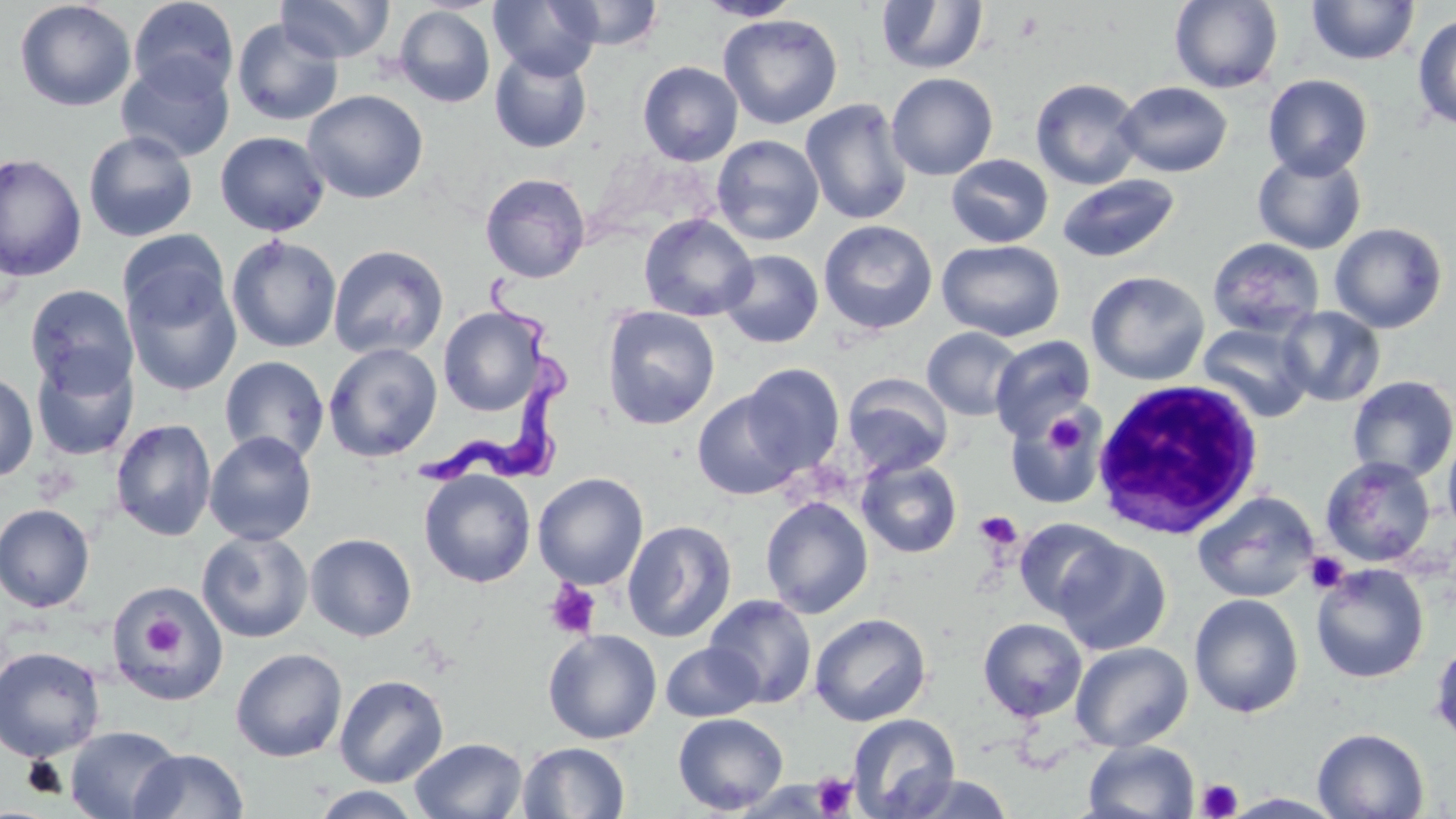
slide_level_diagnosis: Trypanosoma brucei
uninfected_red_blood_cell_locations: 'approximate bounding boxes as (x1, y1, x2, y2) in pixels: (127, 0, 240, 100), (276, 0, 393, 62), (489, 0, 602, 81), (553, 0, 665, 50), (696, 0, 804, 21), (15, 1, 136, 112), (876, 1, 989, 75), (1168, 1, 1284, 93), (1306, 1, 1420, 65), (393, 5, 495, 108), (1412, 12, 1456, 131), (718, 13, 843, 129), (232, 18, 344, 127), (489, 50, 593, 153), (116, 55, 235, 163), (637, 61, 743, 166), (886, 72, 998, 180), (1263, 74, 1373, 179), (1030, 77, 1145, 190), (1115, 81, 1233, 177), (302, 90, 428, 204), (800, 99, 913, 226), (83, 130, 198, 242), (215, 131, 330, 237), (712, 135, 824, 246), (0, 152, 87, 282), (1252, 152, 1367, 254), (945, 154, 1054, 248), (480, 172, 590, 283), (1057, 174, 1180, 264), (639, 213, 758, 322), (819, 220, 938, 335), (1329, 222, 1448, 333), (118, 230, 231, 331), (226, 235, 342, 352), (1207, 237, 1325, 339), (936, 239, 1064, 342), (328, 244, 448, 360), (719, 250, 824, 349), (124, 269, 242, 396), (1086, 270, 1210, 386), (25, 285, 138, 394), (602, 305, 720, 430), (1277, 305, 1387, 407), (438, 306, 548, 416), (1198, 323, 1314, 422), (922, 327, 1023, 420), (989, 335, 1096, 440), (323, 342, 442, 462), (31, 351, 139, 462), (218, 356, 330, 463), (740, 363, 845, 475), (0, 371, 38, 483), (841, 373, 953, 478), (1347, 375, 1456, 482), (692, 390, 804, 501), (1005, 411, 1105, 510), (110, 419, 217, 541), (204, 430, 317, 546), (1442, 432, 1456, 536), (1320, 456, 1436, 567), (856, 458, 963, 558), (419, 469, 536, 588), (532, 473, 649, 590), (1192, 491, 1319, 603), (760, 496, 874, 618), (0, 503, 95, 612), (1013, 517, 1124, 621), (622, 519, 737, 643), (197, 529, 313, 643), (305, 533, 417, 641), (1054, 538, 1171, 656), (1311, 562, 1429, 684), (106, 577, 232, 705), (1189, 593, 1304, 718), (704, 594, 817, 709), (809, 613, 931, 726), (978, 617, 1087, 722), (543, 628, 662, 744), (1429, 637, 1456, 747), (660, 642, 764, 722), (1071, 642, 1193, 752), (0, 645, 107, 762), (230, 647, 348, 762), (334, 674, 449, 787), (673, 712, 789, 815), (848, 714, 960, 819), (64, 724, 183, 819), (1312, 727, 1429, 818), (411, 737, 528, 819), (1083, 740, 1200, 819), (517, 741, 630, 819), (129, 748, 250, 818), (895, 773, 1015, 818), (310, 786, 424, 818)'
trypanosoma_brucei_locations: 'approximate bounding boxes as (x1, y1, x2, y2) in pixels: (421, 267, 578, 490)'
white_blood_cell_locations: 'approximate bounding boxes as (x1, y1, x2, y2) in pixels: (1091, 376, 1266, 539)'
modality: light microscopy
platelet_locations: 'approximate bounding boxes as (x1, y1, x2, y2) in pixels: (1041, 408, 1094, 458), (974, 511, 1023, 550), (1305, 551, 1349, 594), (543, 579, 602, 640), (137, 611, 190, 662), (812, 772, 856, 817), (1197, 779, 1242, 819)'
field_of_view: one of a larger specimen
image_size: 1456×819 pixels
preparation: thin blood smear
magnification: 1000x
stain: May-Grünwald-Giemsa